Assess this cell for malaria.
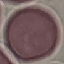

It is uninfected.

capture = smartphone through the microscope eyepiece
stain = Giemsa
preparation = thin blood smear
image type = cell patch, automatically extracted from a larger field of view and resized to 64 × 64 pixels